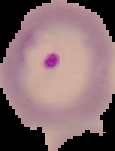

image_type: segmented cell region on a black background
image_size: 115×151 pixels
result: Plasmodium parasites identified
preparation: thin blood film